Comment on the morphology of the red blood cells.
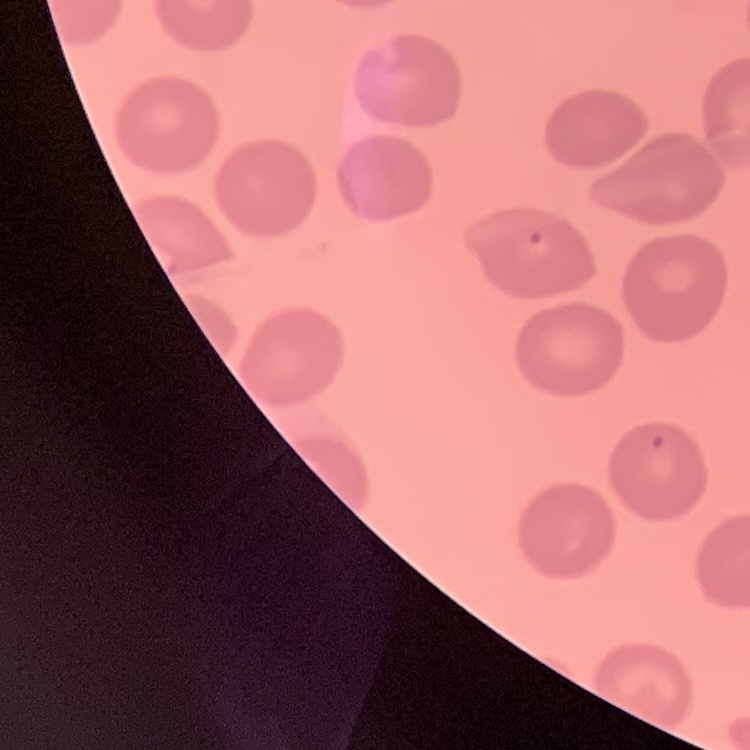
No rouleaux formation.

{
  "image_type": "one tile cut from a larger photomicrograph",
  "preparation": "thin blood film",
  "stain": "Field's or Giemsa"
}